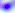 400x magnification. Toxoplasma gondii is shown. Photomicrograph.